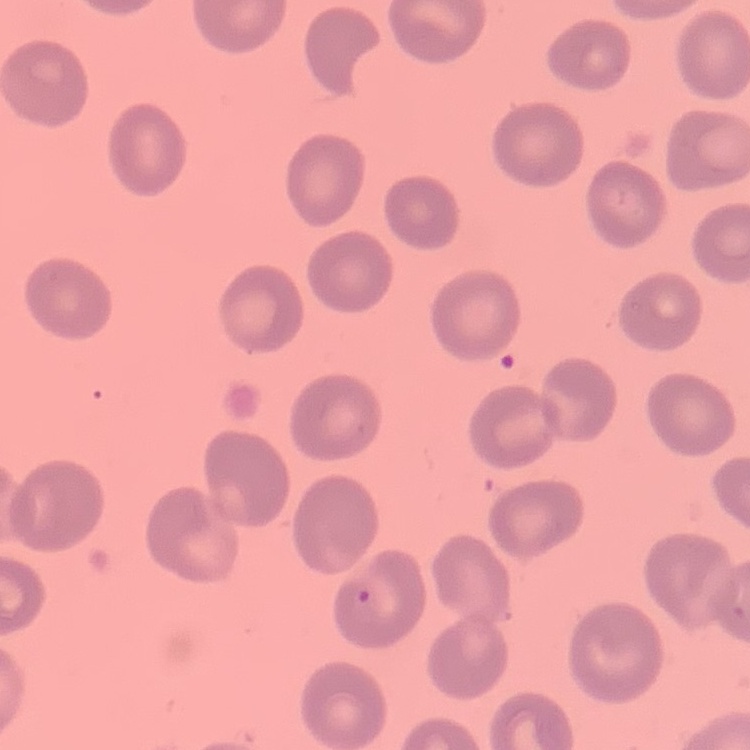 The red blood cells exhibit no rouleaux formation. Stained with either Field's or Giemsa. One tile cut from a larger photomicrograph. Thin blood smear.